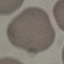
{
  "malaria_status": "uninfected",
  "image_type": "cell patch, automatically extracted from a larger field of view and resized to 64 × 64 pixels",
  "capture": "smartphone camera at the microscope eyepiece",
  "stain": "Giemsa",
  "preparation": "thin blood smear"
}